Locate and identify every blood parasite.
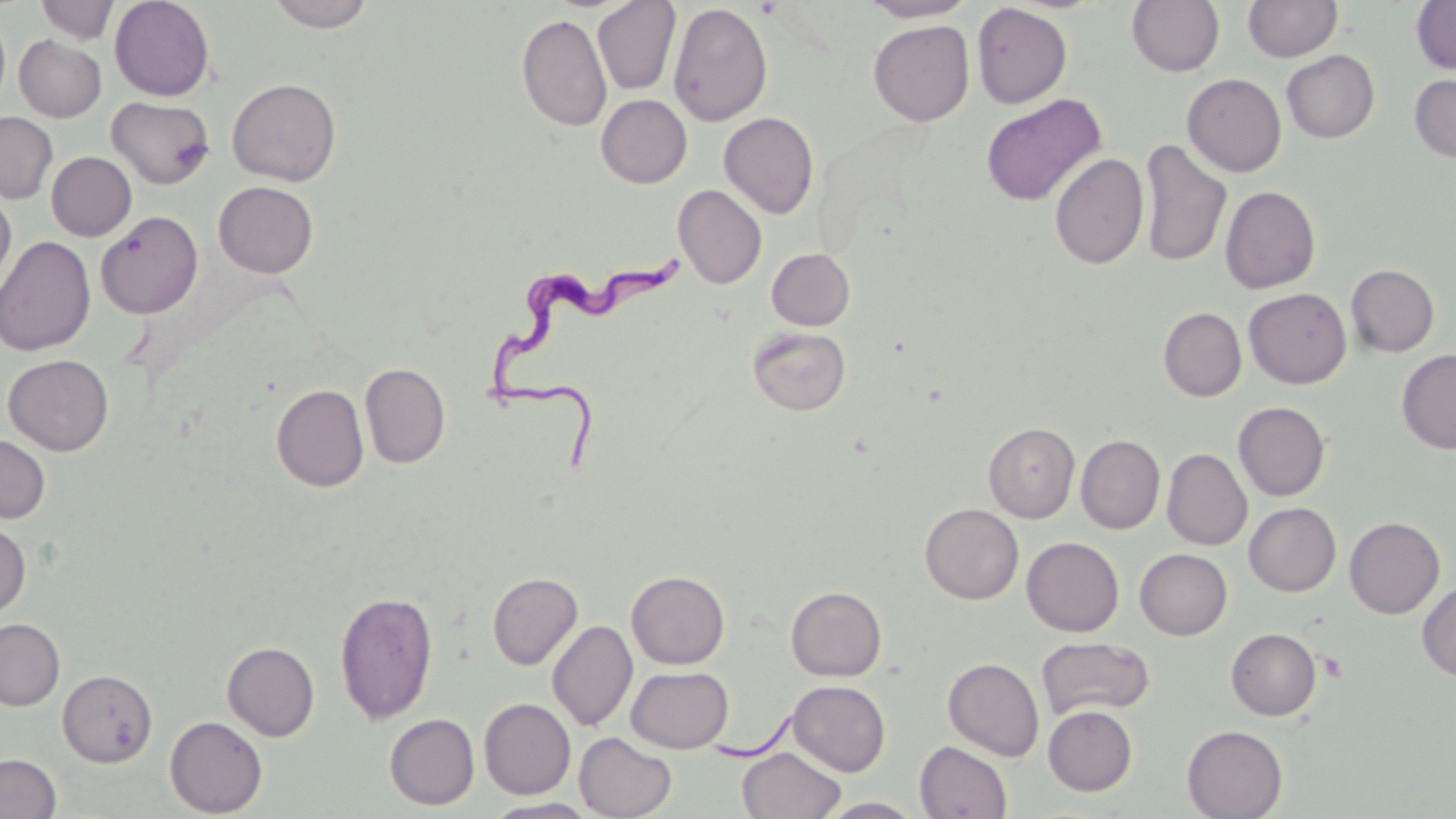
Approximate bounding boxes as (x1, y1, x2, y2) in pixels.
Trypanosoma brucei: (481, 251, 702, 482).
No Plasmodium falciparum, Plasmodium ovale, Plasmodium malariae, Plasmodium vivax, or Babesia divergens observed.

slide-level diagnosis = Trypanosoma brucei
magnification = 1000x
field of view = one of a larger specimen
stain = May-Grünwald-Giemsa
image size = 1456×819 pixels
uninfected red blood cell locations = approximate bounding boxes as (x1, y1, x2, y2) in pixels: (36, 0, 118, 43), (109, 0, 215, 101), (266, 0, 377, 32), (859, 0, 975, 22), (1126, 0, 1224, 76), (1243, 0, 1343, 62), (593, 1, 680, 95), (1410, 1, 1456, 74), (668, 2, 772, 126), (971, 3, 1072, 108), (0, 11, 11, 113), (516, 13, 611, 132), (868, 20, 974, 126), (14, 35, 106, 122), (1282, 50, 1380, 143), (1182, 73, 1286, 177), (1409, 73, 1456, 163), (227, 78, 342, 186), (596, 94, 692, 188), (980, 94, 1107, 207), (106, 97, 215, 189), (0, 112, 58, 204), (719, 112, 819, 219), (1139, 138, 1231, 269), (46, 152, 136, 241), (1049, 153, 1148, 269), (213, 181, 318, 278), (673, 184, 766, 289), (1220, 185, 1321, 294), (0, 190, 16, 296), (95, 211, 203, 319), (0, 235, 96, 356), (766, 248, 855, 330), (1346, 264, 1439, 356), (1244, 287, 1351, 389), (1158, 307, 1247, 402), (747, 325, 851, 416), (1396, 349, 1456, 453), (3, 354, 114, 456), (359, 362, 450, 469), (271, 384, 368, 492), (1233, 401, 1331, 501), (983, 422, 1080, 522), (0, 433, 50, 524), (1076, 434, 1165, 534), (1162, 448, 1252, 551), (920, 503, 1023, 604), (1244, 503, 1340, 596), (1344, 516, 1444, 619), (0, 521, 31, 619), (1022, 536, 1124, 636), (1135, 548, 1232, 640), (626, 570, 730, 669), (487, 572, 583, 670), (1417, 581, 1456, 682), (785, 586, 887, 681), (334, 590, 438, 725), (0, 618, 64, 710), (547, 619, 637, 732), (1226, 628, 1322, 720), (1036, 637, 1155, 722), (222, 641, 319, 740), (943, 657, 1044, 761), (625, 665, 733, 753), (57, 669, 158, 767), (788, 680, 890, 776), (479, 698, 575, 799), (1043, 705, 1137, 795), (384, 713, 479, 809), (165, 716, 267, 817), (1182, 725, 1288, 819), (574, 732, 677, 818), (915, 741, 1013, 819), (737, 747, 846, 819), (0, 753, 61, 818), (817, 797, 925, 818), (483, 798, 600, 818)
preparation = thin blood film
modality = optical microscopy